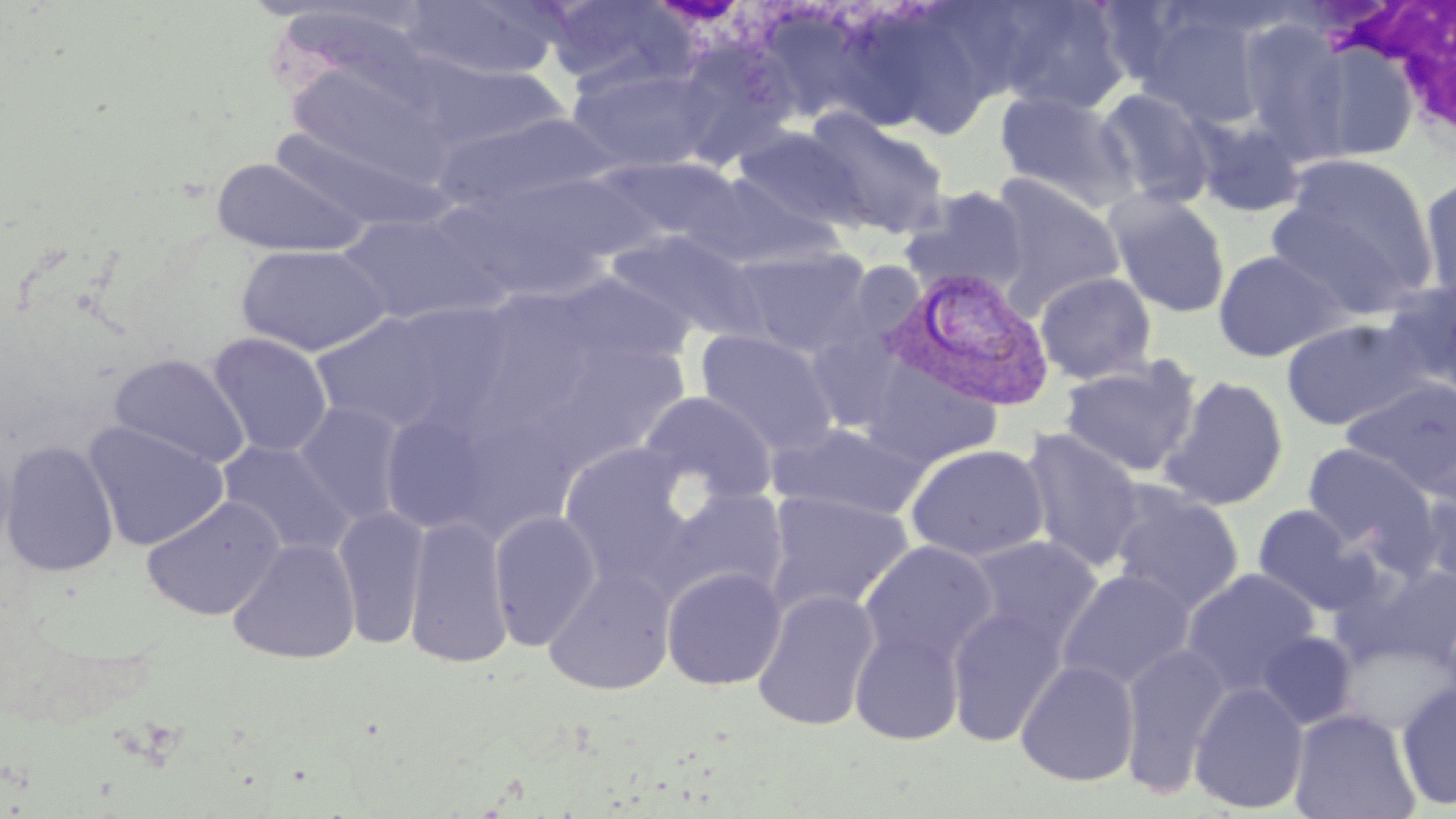

slide-level diagnosis = Plasmodium vivax
uninfected red blood cell locations = approximate bounding boxes as (x1, y1, x2, y2) in pixels: (401, 0, 561, 81), (543, 0, 694, 94), (991, 1, 1132, 115), (264, 5, 445, 102), (1135, 7, 1270, 129), (768, 10, 900, 133), (851, 13, 985, 141), (1237, 17, 1355, 160), (680, 37, 796, 175), (1301, 41, 1422, 163), (424, 62, 571, 151), (567, 64, 718, 174), (1095, 88, 1216, 208), (995, 91, 1137, 211), (802, 108, 950, 239), (435, 113, 618, 215), (1190, 113, 1307, 218), (731, 126, 866, 232), (269, 129, 459, 234), (1266, 154, 1440, 316), (211, 156, 368, 258), (597, 157, 747, 251), (445, 170, 649, 298), (689, 171, 839, 272), (988, 176, 1127, 307), (1418, 176, 1456, 307), (900, 186, 1029, 297), (1106, 191, 1231, 318), (337, 212, 495, 325), (605, 229, 769, 345), (236, 243, 391, 357), (733, 247, 873, 357), (1212, 249, 1348, 361), (1035, 271, 1157, 384), (553, 273, 694, 371), (1382, 278, 1455, 398), (309, 308, 483, 436), (1280, 317, 1433, 431), (695, 329, 839, 456), (207, 332, 333, 458), (108, 353, 250, 469), (1059, 357, 1202, 478), (859, 364, 1007, 470), (1157, 374, 1290, 510), (1341, 378, 1456, 497), (639, 392, 778, 506), (293, 402, 408, 525), (379, 409, 498, 536), (83, 420, 229, 552), (768, 422, 928, 520), (1021, 428, 1145, 573), (0, 439, 119, 577), (217, 440, 357, 560), (1300, 442, 1438, 561), (558, 443, 696, 587), (904, 443, 1050, 562), (1413, 481, 1456, 598), (1109, 485, 1244, 615), (661, 488, 789, 603), (764, 491, 915, 616), (142, 496, 285, 620), (1251, 504, 1376, 616), (332, 505, 429, 650), (488, 510, 601, 650), (404, 516, 514, 668), (964, 535, 1103, 655), (227, 538, 361, 664), (858, 540, 997, 667), (1338, 559, 1456, 671), (543, 564, 677, 695), (661, 566, 787, 690), (1181, 567, 1321, 697), (1056, 568, 1195, 690), (752, 590, 881, 731), (946, 604, 1068, 746), (850, 625, 966, 745), (1256, 630, 1358, 729), (1118, 642, 1231, 798), (1016, 659, 1140, 786), (1189, 681, 1309, 814), (1396, 681, 1456, 810), (1288, 708, 1420, 819)
magnification = 1000x
image size = 1456×819 pixels
stain = May-Grünwald-Giemsa
modality = optical microscopy
white blood cell locations = approximate bounding boxes as (x1, y1, x2, y2) in pixels: (1335, 3, 1455, 129)
field of view = single
Plasmodium vivax-infected red blood cell locations = approximate bounding boxes as (x1, y1, x2, y2) in pixels: (878, 267, 1057, 413)
preparation = thin blood film